Locate every uninfected red blood cell.
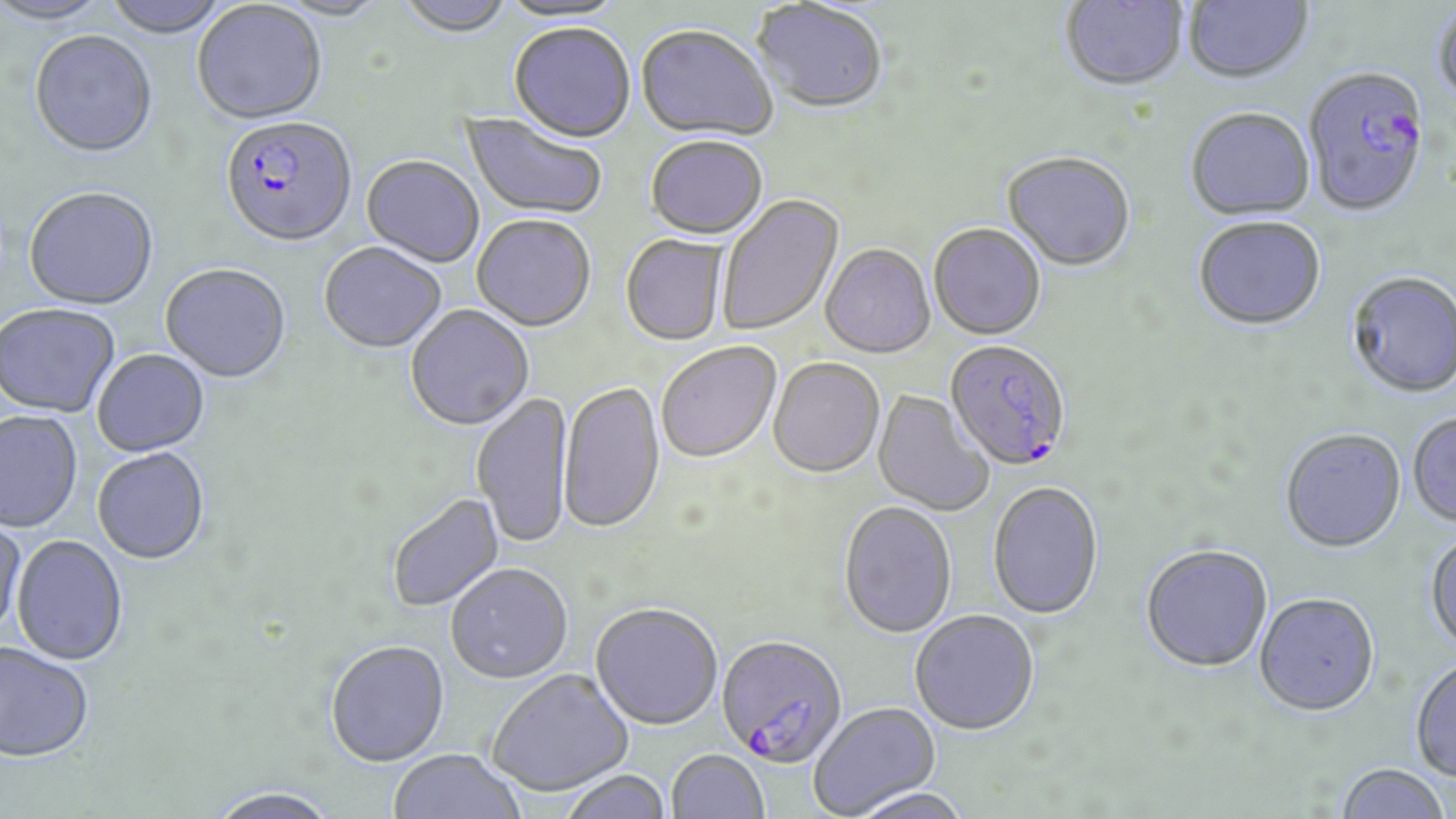
Approximate bounding boxes as (x1,y1)-(x2,y2) corner pairs in pixels.
Uninfected red blood cells: (1,0)-(113,27), (103,0)-(232,39), (395,0)-(516,39), (496,0)-(630,25), (1060,0)-(1189,94), (1183,0)-(1314,87), (751,2)-(888,117), (191,3)-(327,127), (1433,4)-(1456,110), (509,25)-(635,145), (636,26)-(777,144), (29,34)-(158,161), (1185,110)-(1316,223), (459,112)-(607,222), (646,139)-(768,241), (1001,154)-(1136,274), (361,157)-(484,269), (23,189)-(159,312), (717,194)-(845,337), (472,216)-(596,334), (1193,219)-(1328,333), (929,226)-(1046,342), (620,235)-(728,347), (319,244)-(447,355), (820,245)-(936,360), (160,266)-(291,385), (1345,273)-(1456,401), (0,305)-(120,419), (405,306)-(535,433), (657,342)-(782,465), (92,351)-(210,458), (768,359)-(885,480), (559,382)-(665,536), (872,390)-(994,517), (471,392)-(574,551), (0,412)-(83,534), (1407,414)-(1456,529), (1280,430)-(1406,555), (92,450)-(209,566), (988,484)-(1104,622), (387,493)-(505,613), (839,503)-(957,640), (0,515)-(27,644), (1425,530)-(1456,656), (11,536)-(128,667), (1140,546)-(1273,675), (445,565)-(573,686), (1254,595)-(1380,719), (589,605)-(723,733), (910,612)-(1040,737), (325,642)-(450,770), (0,643)-(95,765), (1409,657)-(1456,784), (487,671)-(635,799), (808,703)-(942,818), (389,751)-(525,819), (667,751)-(769,818), (1335,763)-(1449,819), (561,772)-(671,819), (206,788)-(342,819), (848,788)-(973,819).

Plasmodium falciparum-infected red blood cell locations = approximate bounding boxes as (x1,y1)-(x2,y2) corner pairs in pixels: (1303,69)-(1431,219), (220,118)-(358,250), (945,342)-(1071,473), (715,637)-(847,769)
slide-level diagnosis = Plasmodium falciparum
magnification = 1000x
field of view = single
preparation = thin blood film
modality = light microscopy
image size = 1456×819 pixels
stain = May-Grünwald-Giemsa